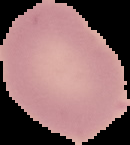

image_type: segmented cell region on a black background
preparation: thin blood smear
malaria_status: uninfected
image_size: 130×145 pixels